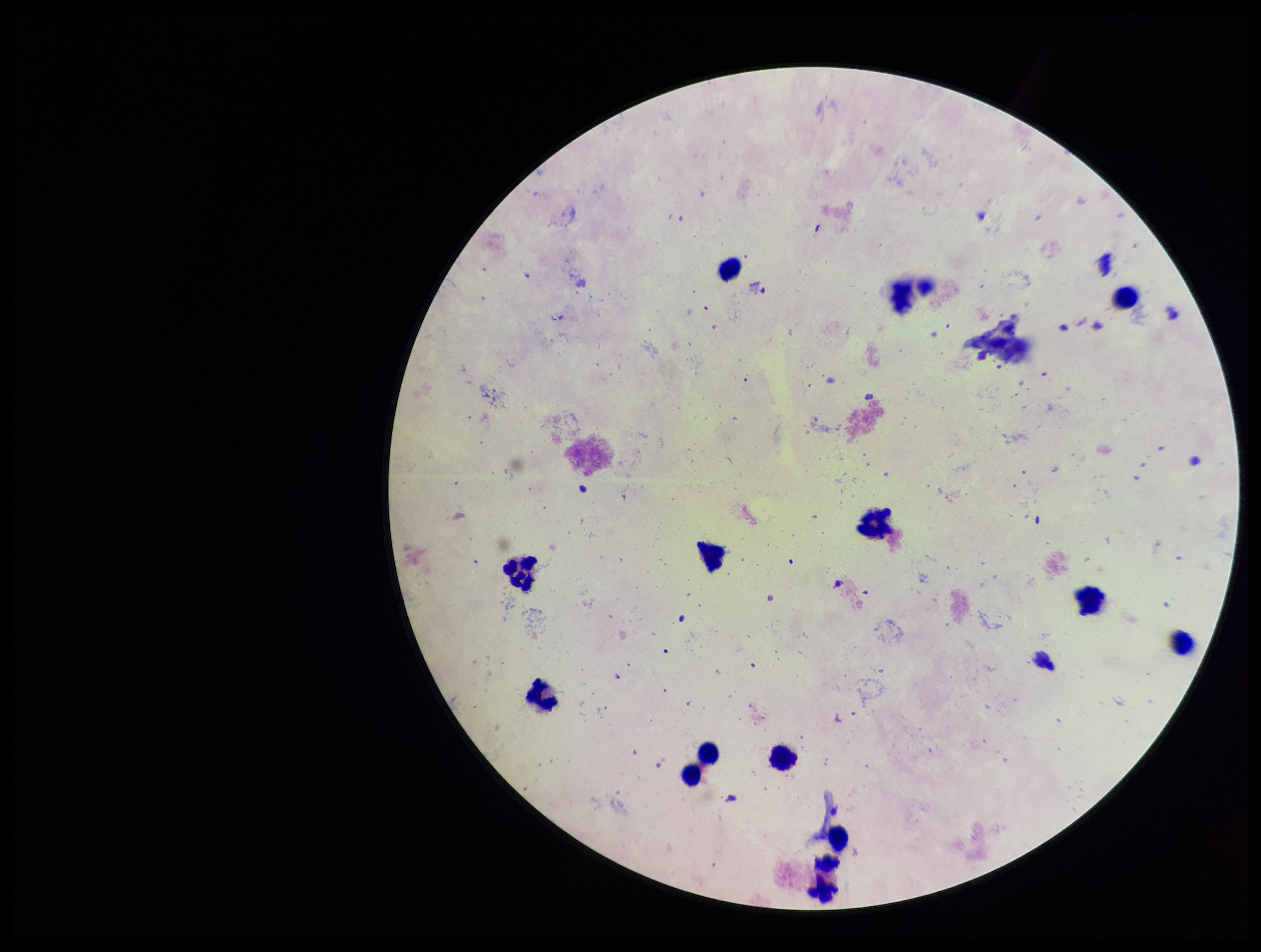
stain = Giemsa
field of view = one from this slide
capture = smartphone photograph through the microscope eyepiece
leukocyte count = 13
parasite count = 0
image size = 1261×952 pixels
Plasmodium parasites = none detected
patient malaria status = negative
preparation = thick smear